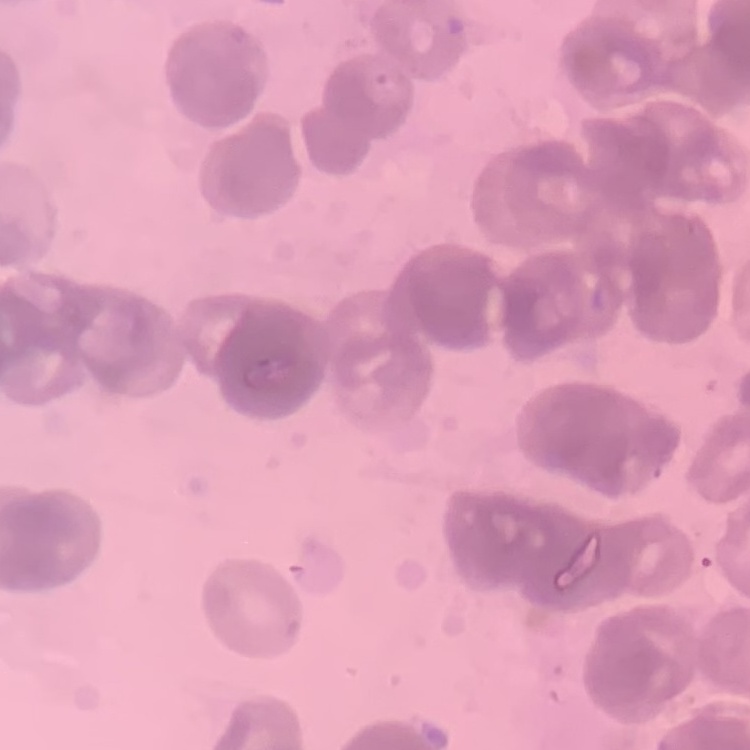

Summary:
  - Erythrocyte morphology: rouleaux formation
  - Image type: square crop of a larger photomicrograph
  - Preparation: thin blood film
  - Stain: Field's or Giemsa